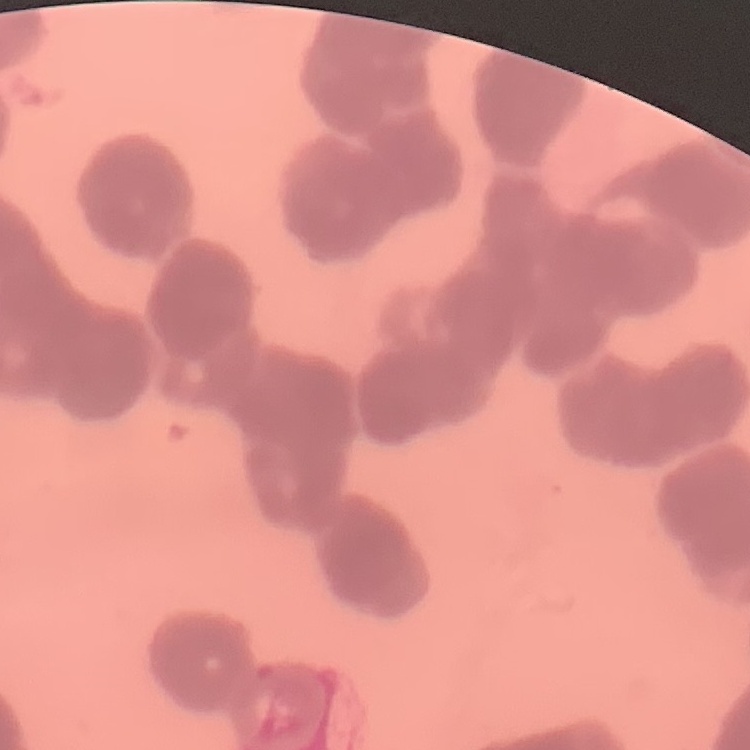 The erythrocytes show rouleaux formation. Thin blood film. Field's or Giemsa stain. Square crop of a larger photomicrograph.